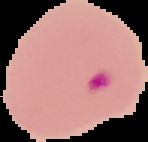
Malaria status: parasitized. Image is 148×142 pixels. The area outside the segmented cell region is set to black. From a thin blood smear.